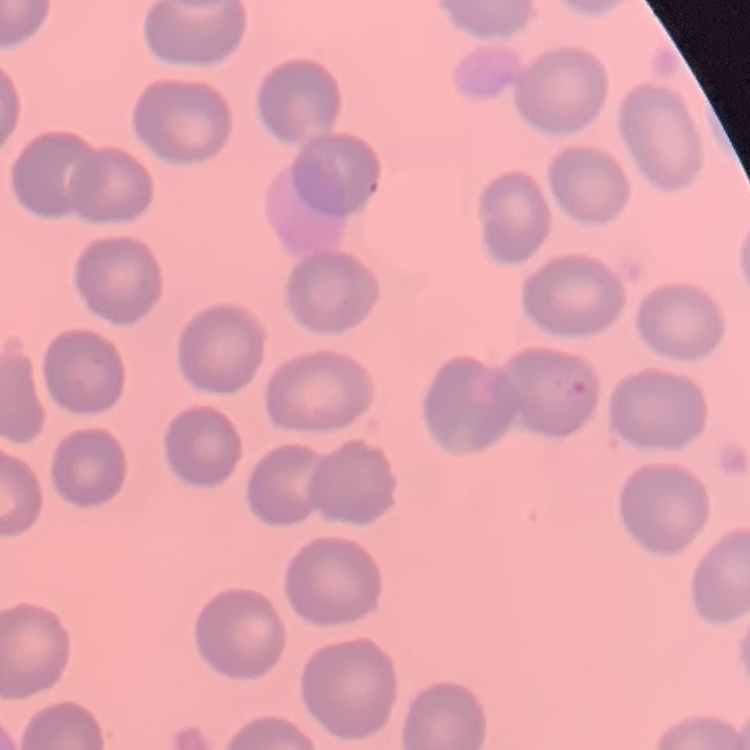

Summary:
  - Erythrocyte morphology: no rouleaux formation
  - Stain: Field's or Giemsa
  - Image type: one tile cut from a larger photomicrograph
  - Preparation: thin peripheral smear